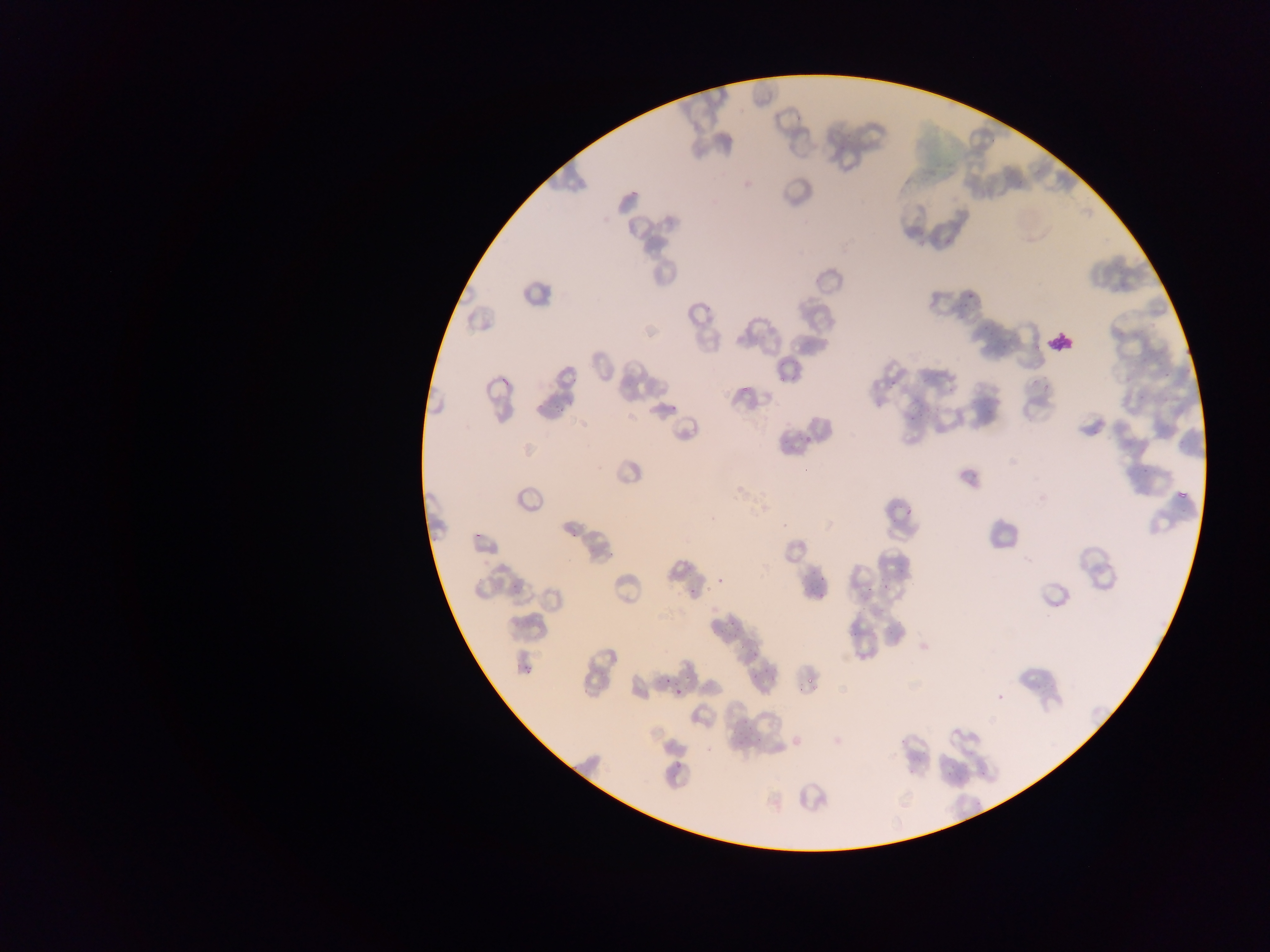 Approximate bounding boxes as {left, top, right, bottom} in pixels. Malaria parasite locations (subset; some below the resolvable size): {964, 288, 973, 301}, {957, 303, 967, 310}, {978, 322, 992, 341}, {996, 332, 1015, 350}, {1135, 334, 1155, 356}, {1160, 365, 1174, 382}, {498, 376, 510, 388}, {888, 378, 897, 391}, {739, 383, 750, 397}, {1133, 391, 1145, 401}, {549, 400, 563, 417}, {906, 410, 926, 423}, {795, 427, 814, 448}, {1128, 461, 1158, 474}, {1176, 489, 1189, 502}, {900, 497, 913, 525}, {568, 528, 581, 539}, {474, 529, 487, 539}, {605, 547, 617, 557}, {814, 566, 831, 584}, {508, 574, 519, 589}, {886, 577, 896, 590}, {859, 587, 873, 598}, {689, 591, 701, 596}, {812, 593, 823, 604}, {722, 619, 740, 629}, {749, 647, 764, 660}, {525, 664, 534, 678}, {753, 664, 767, 679}, {662, 674, 673, 689}, {804, 676, 816, 691}, {674, 688, 682, 698}, {732, 721, 747, 740}, {952, 729, 960, 736}, {753, 733, 768, 747}, {672, 756, 684, 777}. Single field of view. Mobile-phone photograph taken through the microscope. Collected in Ghana. Image is 1270×952 pixels. Thin blood smear.